Assess this cell for malaria.
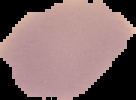

It is uninfected.

preparation = thin blood smear
image size = 136×100 pixels
image type = cell region segmented out of the field of view; surrounding area masked to black